Give the extent of all Plasmodium falciparum-infected red blood cells.
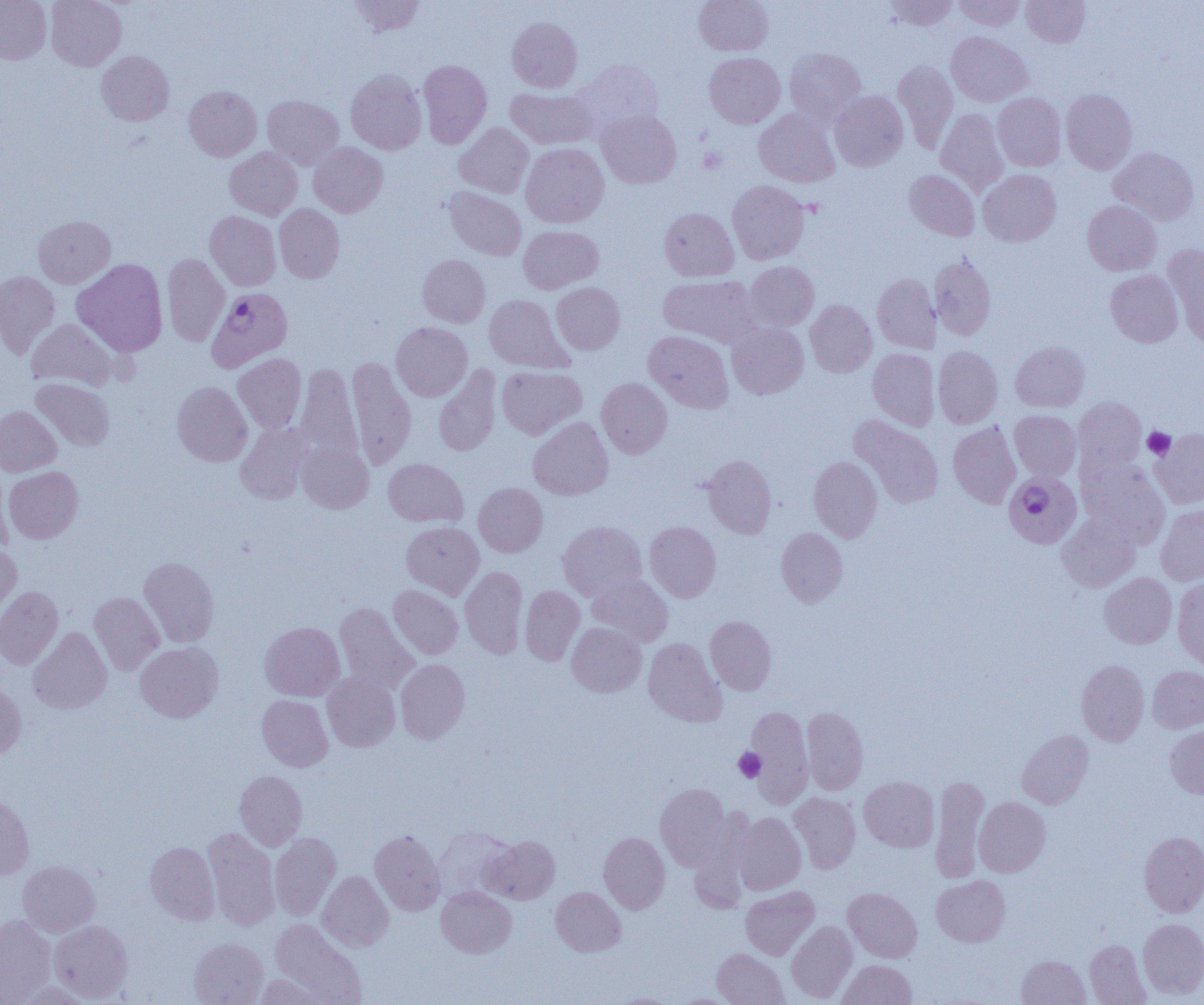

Approximate bounding boxes as (x1,y1)-(x2,y2) corner pairs in pixels.
Plasmodium falciparum-infected red blood cells: (210,285)-(291,376), (1004,471)-(1082,548).

{
  "slide_level_diagnosis": "Plasmodium falciparum",
  "magnification": "1000x",
  "uninfected_red_blood_cell_locations": "approximate bounding boxes as (x1,y1)-(x2,y2) corner pairs in pixels: (0,0)-(52,64), (46,0)-(126,71), (347,0)-(426,37), (694,0)-(773,55), (885,0)-(958,30), (954,0)-(1026,31), (1021,0)-(1090,47), (507,17)-(582,92), (946,31)-(1033,106), (784,47)-(867,127), (96,50)-(174,126), (704,52)-(785,128), (418,59)-(492,148), (893,59)-(958,153), (575,60)-(664,134), (346,68)-(426,154), (184,86)-(262,161), (506,87)-(596,149), (1061,88)-(1138,174), (830,90)-(908,171), (993,92)-(1066,171), (263,95)-(344,169), (754,109)-(840,187), (935,109)-(1009,194), (597,110)-(681,188), (454,123)-(534,198), (309,142)-(387,217), (521,143)-(609,228), (224,147)-(303,220), (1108,147)-(1199,225), (904,169)-(980,241), (978,169)-(1061,246), (727,180)-(809,264), (445,187)-(526,261), (1083,201)-(1161,275), (274,204)-(344,283), (659,207)-(739,282), (205,211)-(280,291), (33,215)-(115,288), (518,225)-(603,294), (1163,245)-(1204,345), (162,253)-(230,346), (928,253)-(996,341), (417,255)-(490,327), (72,259)-(168,357), (744,261)-(819,332), (1105,270)-(1183,347), (0,271)-(60,359), (872,273)-(941,354), (658,274)-(762,347), (551,282)-(624,354), (484,294)-(571,373), (805,299)-(877,377), (27,319)-(119,391), (391,322)-(472,401), (727,323)-(809,399), (644,330)-(734,413), (1011,341)-(1089,411), (933,346)-(1003,429), (868,348)-(940,431), (233,353)-(306,433), (347,357)-(416,470), (295,362)-(361,465), (433,365)-(502,457), (497,366)-(586,439), (32,378)-(115,451), (596,378)-(672,458), (172,381)-(252,466), (1073,396)-(1147,478), (0,405)-(62,476), (1009,410)-(1081,481), (849,415)-(944,508), (528,417)-(613,500), (235,421)-(314,504), (948,422)-(1021,508), (1151,428)-(1204,508), (296,440)-(374,513), (702,455)-(776,538), (808,456)-(883,542), (383,458)-(467,527), (1078,459)-(1170,548), (3,466)-(83,543), (0,469)-(14,553), (473,483)-(548,557), (1156,505)-(1204,586), (1057,513)-(1141,591), (401,521)-(484,598), (558,521)-(647,601), (644,521)-(721,602), (776,527)-(848,607), (0,544)-(21,625), (139,556)-(219,647), (460,566)-(527,658), (1099,572)-(1177,649), (587,573)-(673,646), (1172,575)-(1204,671), (388,585)-(463,659), (0,586)-(63,669), (520,586)-(585,665), (89,592)-(164,675), (334,602)-(418,693), (705,615)-(777,695), (260,621)-(345,701), (567,622)-(646,697), (28,627)-(111,714), (643,638)-(726,727), (135,641)-(223,722), (396,658)-(470,744), (1076,660)-(1149,746), (1147,666)-(1204,733), (322,671)-(400,752), (0,683)-(26,760), (257,695)-(332,771), (745,705)-(814,806), (801,707)-(868,794), (1165,725)-(1204,799), (1016,729)-(1094,809), (234,770)-(307,850), (930,776)-(990,882), (859,777)-(939,852), (655,783)-(731,869), (789,792)-(861,874), (0,795)-(34,879), (974,796)-(1050,877), (734,812)-(806,894), (203,827)-(280,930), (434,827)-(517,902), (370,830)-(445,915), (1139,831)-(1204,917), (599,832)-(670,914), (270,833)-(340,919), (485,835)-(560,904), (146,842)-(219,924), (18,860)-(99,937), (317,871)-(394,952), (932,875)-(1010,947), (436,886)-(516,958), (740,886)-(819,960), (551,887)-(625,956), (843,888)-(922,962), (0,914)-(56,1002), (271,918)-(364,1001), (1138,918)-(1204,999), (49,920)-(133,1002), (786,921)-(857,1002), (189,938)-(267,1005), (1085,939)-(1150,1004), (712,948)-(788,1005), (1016,955)-(1090,1004), (837,959)-(916,1005), (254,973)-(334,1004), (14,982)-(92,1005), (611,994)-(679,1005), (671,994)-(737,1004)",
  "field_of_view": "single",
  "modality": "light microscopy",
  "preparation": "thin blood film",
  "image_size": "1204×1005 pixels",
  "platelet_locations": "approximate bounding boxes as (x1,y1)-(x2,y2) corner pairs in pixels: (699,147)-(727,174), (1143,427)-(1175,460), (733,748)-(766,782)"
}